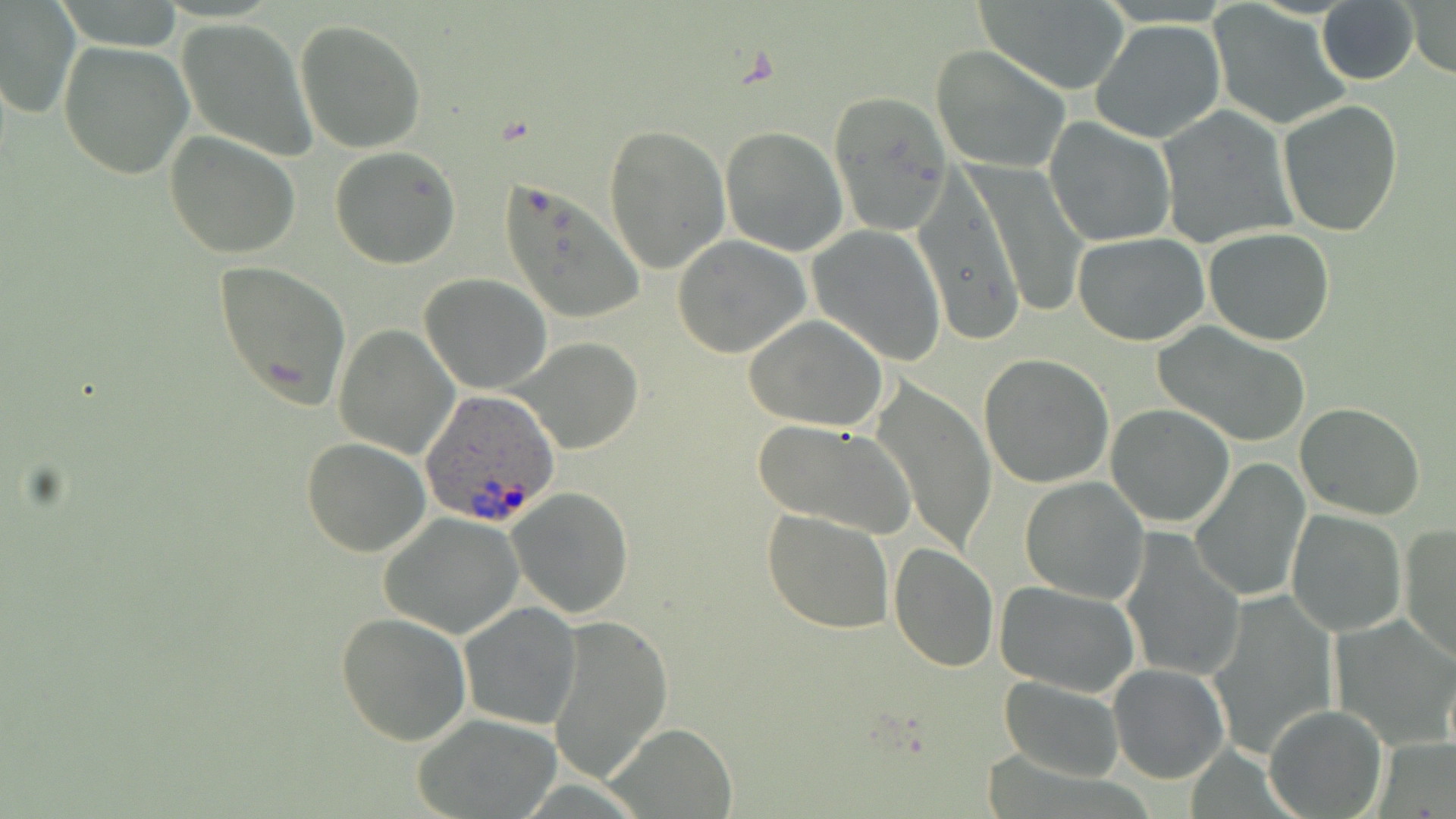
{
  "slide_level_diagnosis": "Plasmodium ovale",
  "magnification": "1000x",
  "uninfected_red_blood_cell_locations": "approximate bounding boxes as (x1, y1, x2, y2) in pixels: (1405, 0, 1456, 77), (0, 1, 79, 120), (1205, 2, 1349, 131), (977, 3, 1129, 90), (1318, 3, 1418, 84), (176, 19, 316, 158), (294, 19, 427, 155), (1090, 19, 1226, 144), (58, 39, 195, 180), (931, 43, 1074, 174), (829, 90, 954, 234), (1277, 101, 1403, 236), (1158, 107, 1297, 246), (1044, 116, 1177, 247), (604, 124, 730, 273), (720, 126, 848, 256), (165, 131, 301, 260), (330, 145, 461, 268), (964, 160, 1087, 319), (913, 169, 1027, 344), (501, 181, 644, 326), (807, 224, 947, 365), (1204, 228, 1336, 346), (672, 234, 811, 358), (1073, 234, 1209, 346), (212, 259, 352, 410), (420, 273, 552, 394), (743, 314, 889, 432), (334, 323, 457, 458), (1154, 323, 1312, 447), (514, 337, 644, 455), (979, 353, 1114, 488), (870, 380, 996, 552), (1296, 401, 1425, 519), (1104, 404, 1235, 529), (753, 419, 914, 538), (301, 437, 430, 556), (1191, 455, 1311, 603), (1020, 476, 1149, 606), (508, 487, 634, 617), (761, 507, 894, 632), (1284, 509, 1407, 635), (379, 513, 524, 637), (1400, 523, 1456, 664), (1118, 530, 1242, 679), (888, 542, 1000, 673), (994, 581, 1141, 696), (1203, 590, 1338, 761), (457, 600, 582, 731), (336, 612, 473, 746), (547, 613, 672, 784), (1331, 613, 1456, 748), (1108, 663, 1228, 783), (998, 675, 1125, 780), (1263, 703, 1387, 818), (414, 713, 564, 818), (603, 726, 735, 816)",
  "preparation": "thin blood film",
  "image_size": "1456×819 pixels",
  "stain": "May-Grünwald-Giemsa",
  "plasmodium_ovale_infected_red_blood_cell_locations": "approximate bounding boxes as (x1, y1, x2, y2) in pixels: (419, 389, 560, 528)",
  "field_of_view": "one of a larger specimen",
  "modality": "light microscopy"
}